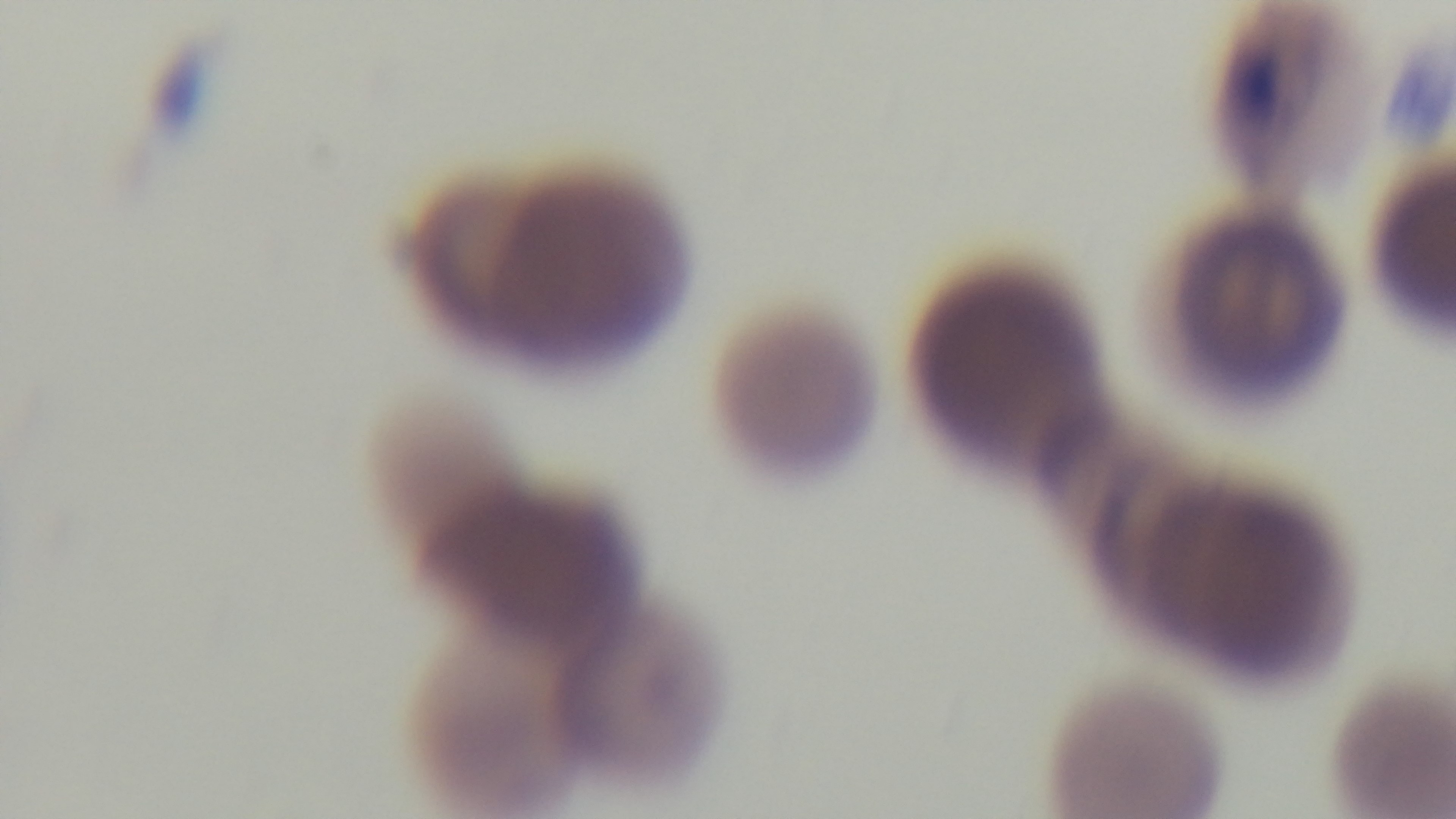

Summary:
  - Preparation: thin smear
  - Capture: mounted 4K digital camera
  - Stain: Giemsa
  - Malaria status: infected
  - Modality: light microscopy
  - Objective: 100x oil immersion
  - Field of view: single